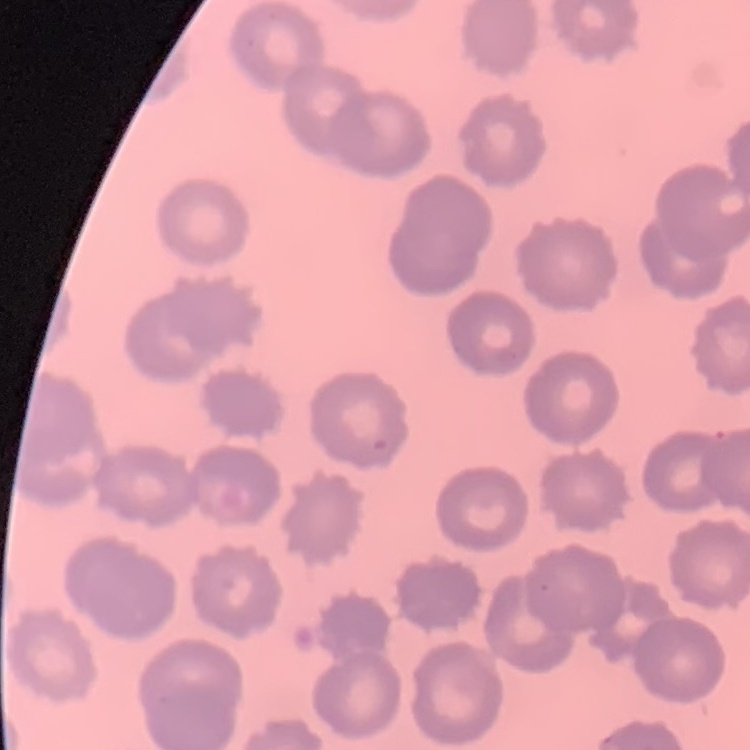 The erythrocytes exhibit no rouleaux formation. One tile cut from a larger photomicrograph. Thin peripheral smear. Stained with either Field's or Giemsa.